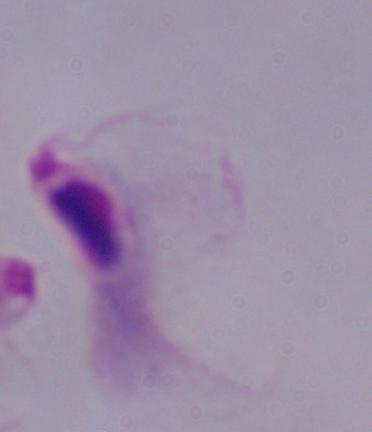

Captured at 1000x magnification. Photomicrograph. A trichomonad is seen.